Locate the cells, classifying each as a parasitized red blood cell, an uninfected red blood cell, or a white blood cell.
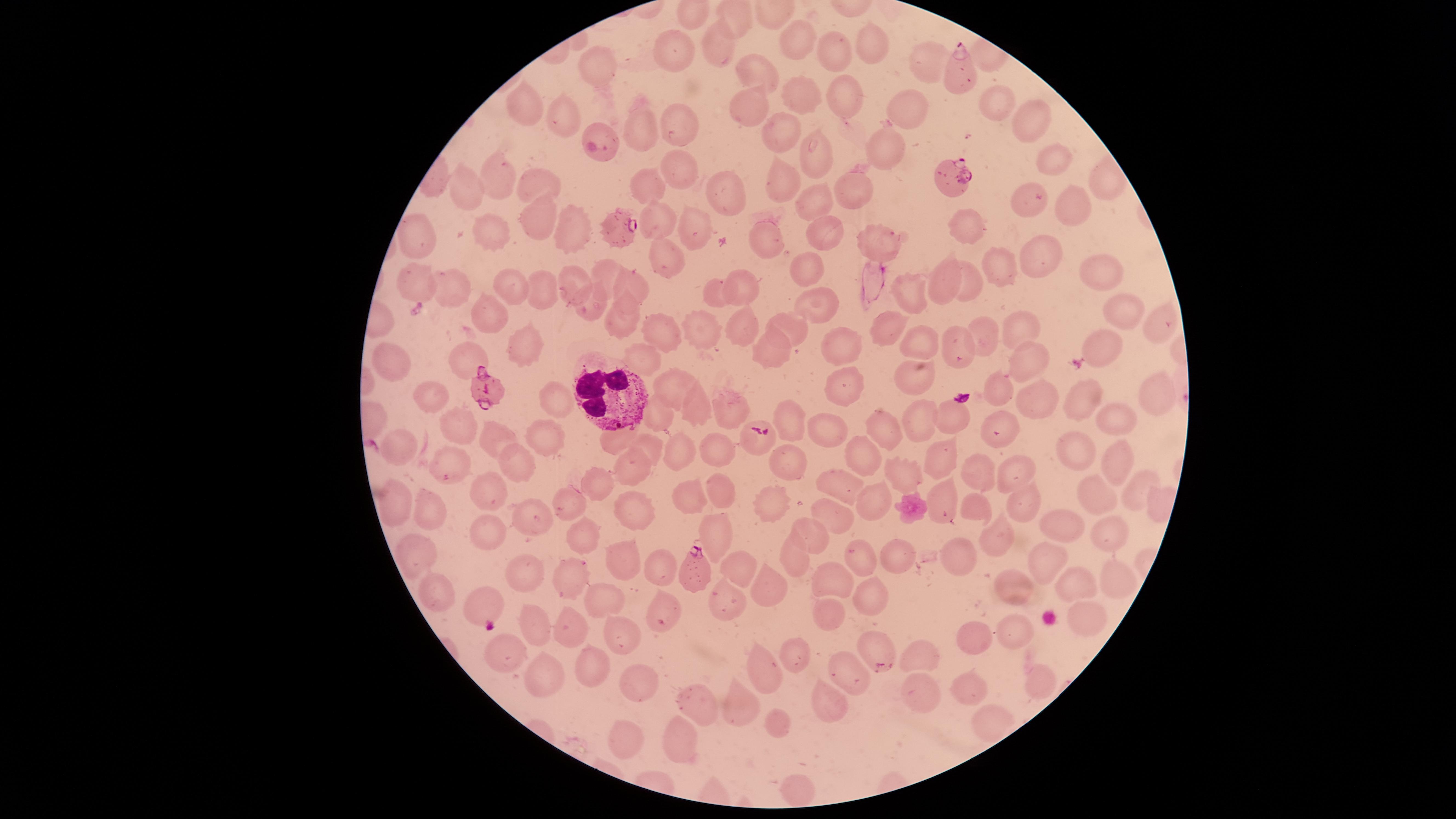

Approximate marker points as {x, y} in pixels.
Parasitized red blood cells: {953, 70}, {952, 177}, {620, 227}, {487, 390}, {695, 574}, {485, 604}.
Uninfected red blood cells: {733, 21}, {796, 40}, {874, 42}, {722, 45}, {833, 47}, {681, 53}, {599, 71}, {758, 72}, {925, 74}, {799, 90}, {842, 92}, {993, 101}, {529, 103}, {907, 104}, {749, 107}, {1028, 117}, {562, 118}, {643, 127}, {599, 129}, {784, 130}, {680, 134}, {888, 142}, {816, 156}, {1050, 160}, {677, 169}, {498, 175}, {783, 181}, {541, 184}, {645, 184}, {726, 189}, {467, 191}, {853, 192}, {811, 201}, {1075, 204}, {1027, 207}, {661, 221}, {537, 223}, {830, 225}, {692, 228}, {966, 230}, {492, 232}, {574, 234}, {770, 235}, {420, 236}, {877, 241}, {1035, 253}, {665, 254}, {996, 263}, {806, 266}, {1100, 270}, {605, 271}, {567, 279}, {947, 279}, {972, 279}, {633, 281}, {417, 282}, {744, 282}, {515, 286}, {910, 287}, {454, 290}, {547, 290}, {716, 292}, {588, 305}, {818, 308}, {625, 314}, {1123, 314}, {492, 315}, {1162, 321}, {880, 326}, {1016, 326}, {663, 328}, {748, 328}, {790, 329}, {696, 331}, {981, 331}, {838, 339}, {921, 342}, {1108, 343}, {524, 344}, {774, 350}, {962, 353}, {648, 359}, {466, 360}, {391, 361}, {1030, 361}, {915, 376}, {842, 381}, {669, 386}, {1152, 388}, {998, 389}, {428, 395}, {1041, 399}, {557, 401}, {1082, 402}, {732, 409}, {696, 411}, {659, 415}, {947, 416}, {1115, 417}, {921, 418}, {793, 420}, {460, 427}, {879, 427}, {998, 427}, {545, 431}, {830, 431}, {497, 437}, {616, 441}, {753, 442}, {647, 443}, {716, 443}, {403, 446}, {1082, 448}, {864, 452}, {680, 454}, {941, 461}, {1116, 462}, {790, 464}, {450, 465}, {1020, 467}, {514, 469}, {628, 470}, {977, 471}, {902, 472}, {843, 484}, {598, 486}, {492, 487}, {725, 487}, {1138, 487}, {1093, 490}, {689, 496}, {767, 496}, {940, 498}, {1021, 498}, {396, 502}, {878, 502}, {430, 503}, {574, 507}, {630, 509}, {979, 511}, {834, 515}, {526, 517}, {1055, 525}, {1114, 532}, {583, 533}, {811, 533}, {489, 535}, {991, 540}, {716, 541}, {862, 553}, {796, 554}, {409, 555}, {895, 556}, {960, 557}, {620, 559}, {742, 564}, {658, 568}, {1041, 570}, {520, 571}, {569, 576}, {1116, 580}, {834, 581}, {1074, 584}, {774, 585}, {435, 587}, {1013, 587}, {872, 596}, {601, 600}, {726, 601}, {830, 612}, {664, 614}, {528, 619}, {1085, 620}, {620, 627}, {567, 629}, {1016, 633}, {972, 638}, {873, 641}, {505, 652}, {914, 653}, {795, 665}, {595, 667}, {761, 675}, {548, 677}, {843, 678}, {1039, 679}, {641, 684}, {970, 692}, {916, 696}, {697, 703}, {741, 705}, {826, 705}, {779, 723}, {677, 744}, {628, 745}, {797, 790}.
White blood cells: {611, 399}.

Summary:
  - Field of view: single
  - Image size: 1456×819 pixels
  - Stain: Giemsa
  - Capture: smartphone photograph through the microscope eyepiece
  - Species: Plasmodium falciparum
  - Visible region: circular
  - Preparation: thin blood film